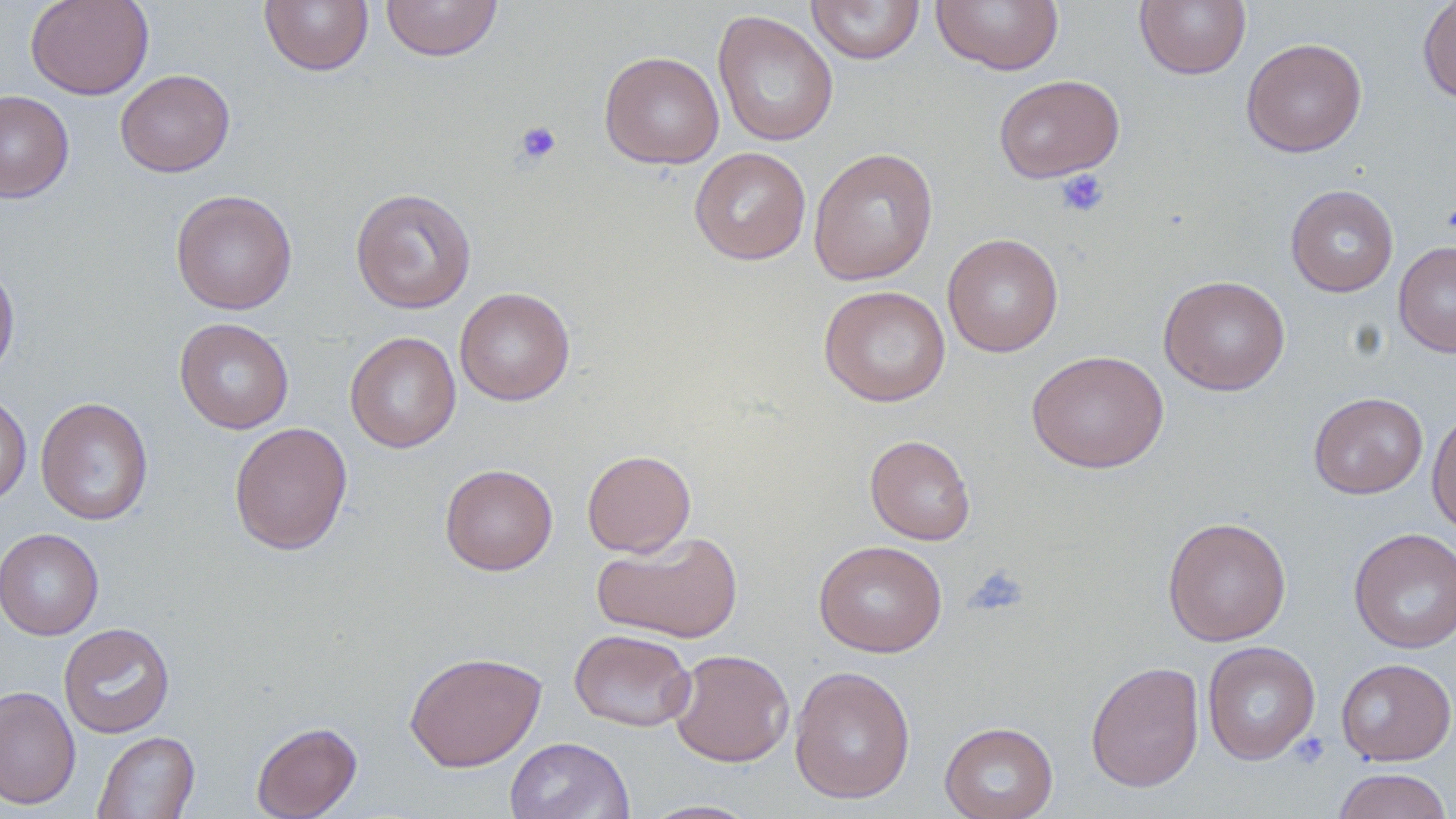
slide-level diagnosis = negative for blood parasites
platelet locations = approximate bounding boxes as (x1,y1)-(x2,y2) corner pairs in pixels: (514,120)-(562,166), (1055,169)-(1110,218), (1441,202)-(1456,238), (965,565)-(1029,616), (1288,733)-(1330,770)
image size = 1456×819 pixels
magnification = 1000x
preparation = thin blood smear
field of view = single
stain = May-Grünwald-Giemsa
modality = light microscopy
uninfected red blood cell locations = approximate bounding boxes as (x1,y1)-(x2,y2) corner pairs in pixels: (25,0)-(154,100), (259,0)-(374,76), (380,0)-(503,62), (807,0)-(925,65), (931,0)-(1064,75), (1135,0)-(1251,80), (1417,0)-(1456,105), (712,10)-(838,146), (1241,38)-(1367,158), (599,50)-(724,169), (115,69)-(235,177), (994,74)-(1125,183), (0,90)-(74,202), (689,147)-(811,265), (808,147)-(938,285), (1285,184)-(1399,297), (350,187)-(477,314), (170,189)-(297,315), (942,233)-(1063,357), (1393,240)-(1456,357), (0,256)-(20,383), (1159,275)-(1291,395), (818,285)-(951,407), (454,287)-(575,406), (174,317)-(294,434), (345,331)-(461,453), (1026,349)-(1168,473), (0,392)-(31,510), (1309,392)-(1428,499), (35,397)-(153,526), (1426,408)-(1456,536), (229,422)-(353,555), (864,434)-(976,545), (581,449)-(696,557), (440,463)-(558,575), (1163,516)-(1291,646), (0,528)-(104,640), (1349,528)-(1456,653), (593,530)-(743,643), (814,539)-(947,657), (59,623)-(175,738), (569,629)-(696,731), (1203,641)-(1320,765), (668,648)-(795,767), (404,650)-(547,772), (1336,658)-(1456,766), (1085,661)-(1205,793), (789,665)-(916,804), (0,685)-(81,810), (251,721)-(362,819), (940,721)-(1058,819), (93,730)-(199,818), (504,736)-(633,819), (1332,768)-(1453,819), (639,799)-(763,818)